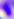
Summary:
  - Magnification: 400x
  - Modality: micrograph
  - Identification: Toxoplasma gondii